Assess this cell for malaria.
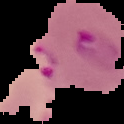
Parasitized.

{
  "image_type": "cell region segmented out of the field of view; surrounding area masked to black",
  "preparation": "thin blood film",
  "image_size": "124×124 pixels"
}